Report the malaria status of this cell.
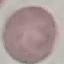
Uninfected.

Photographed with a smartphone camera at the microscope eyepiece. Giemsa-stained preparation. Automatically extracted cell patch, resized to 64 × 64 pixels. Thin blood smear.